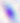

Summary:
  - Modality: micrograph
  - Magnification: 400x
  - Identification: Toxoplasma gondii